Outline each Plasmodium malariae-infected red blood cell.
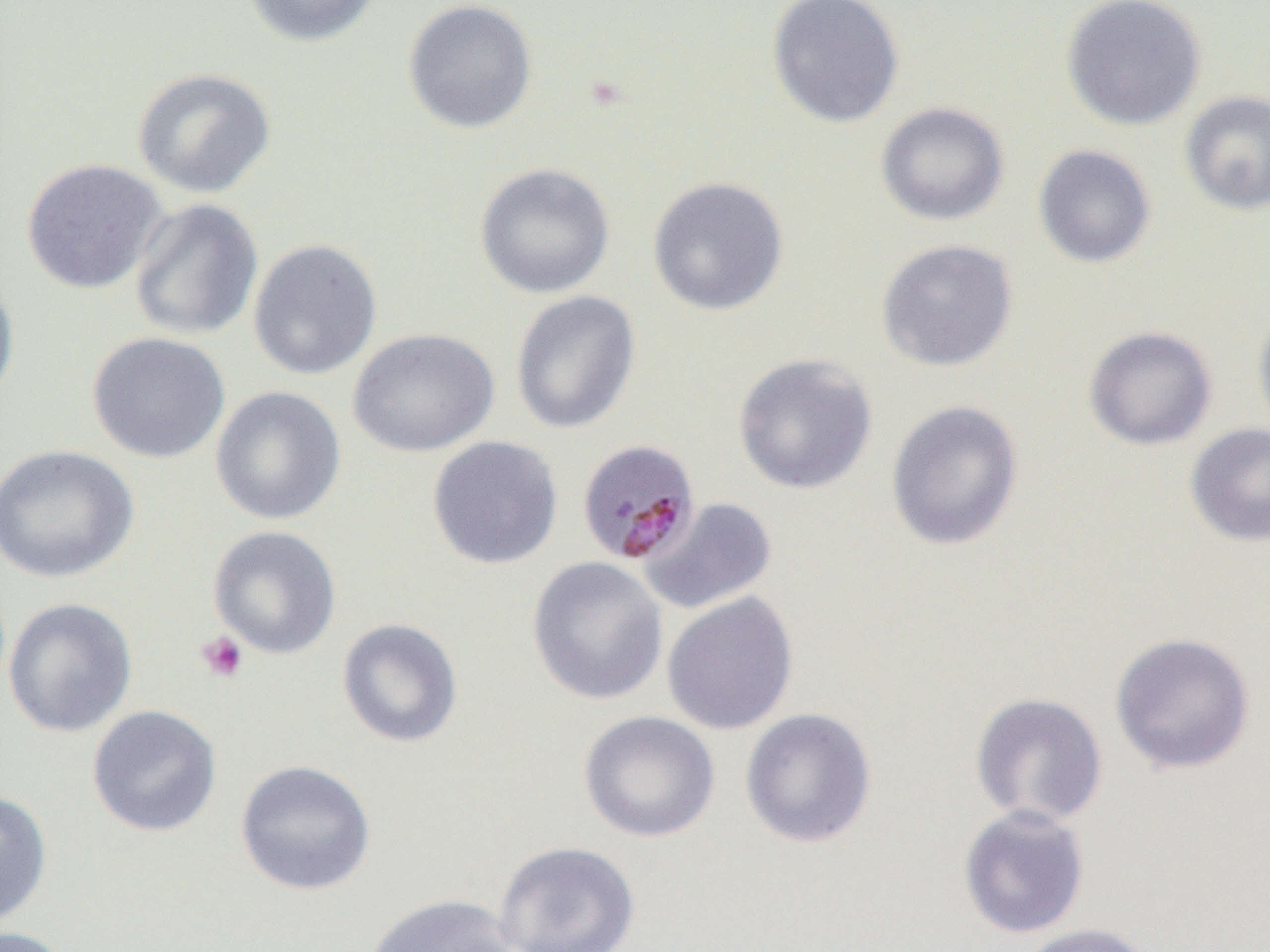
Approximate bounding boxes as named x1/y1/x2/y2 corners in pixels.
Plasmodium malariae-infected red blood cells: (x1=576, y1=438, x2=701, y2=565).

slide-level diagnosis = Plasmodium malariae
preparation = thin blood smear
magnification = 1000x
field of view = one of a larger specimen
image size = 1270×952 pixels
uninfected red blood cell locations = approximate bounding boxes as named x1/y1/x2/y2 corners in pixels: (x1=243, y1=0, x2=383, y2=48), (x1=402, y1=0, x2=538, y2=134), (x1=766, y1=0, x2=905, y2=128), (x1=1060, y1=0, x2=1206, y2=131), (x1=131, y1=67, x2=277, y2=199), (x1=1180, y1=90, x2=1270, y2=217), (x1=875, y1=101, x2=1010, y2=226), (x1=1032, y1=144, x2=1156, y2=268), (x1=21, y1=158, x2=168, y2=294), (x1=473, y1=163, x2=615, y2=299), (x1=647, y1=176, x2=789, y2=316), (x1=129, y1=198, x2=263, y2=341), (x1=248, y1=238, x2=382, y2=380), (x1=876, y1=238, x2=1019, y2=373), (x1=0, y1=271, x2=20, y2=411), (x1=510, y1=291, x2=641, y2=434), (x1=1252, y1=302, x2=1270, y2=440), (x1=1082, y1=325, x2=1217, y2=450), (x1=348, y1=327, x2=500, y2=458), (x1=87, y1=332, x2=231, y2=464), (x1=731, y1=352, x2=878, y2=495), (x1=210, y1=385, x2=347, y2=525), (x1=885, y1=399, x2=1024, y2=551), (x1=1185, y1=423, x2=1270, y2=546), (x1=427, y1=436, x2=563, y2=570), (x1=0, y1=444, x2=138, y2=583), (x1=638, y1=497, x2=779, y2=615), (x1=208, y1=525, x2=342, y2=659), (x1=526, y1=556, x2=668, y2=705), (x1=661, y1=591, x2=799, y2=735), (x1=3, y1=597, x2=138, y2=738), (x1=336, y1=617, x2=464, y2=748), (x1=1109, y1=631, x2=1256, y2=775), (x1=970, y1=692, x2=1108, y2=827), (x1=87, y1=705, x2=222, y2=837), (x1=740, y1=707, x2=877, y2=848), (x1=577, y1=710, x2=721, y2=843), (x1=234, y1=759, x2=376, y2=895), (x1=0, y1=788, x2=53, y2=929), (x1=957, y1=804, x2=1091, y2=940), (x1=493, y1=840, x2=641, y2=952), (x1=365, y1=893, x2=519, y2=952), (x1=1018, y1=922, x2=1154, y2=952), (x1=0, y1=925, x2=75, y2=952)
platelet locations = approximate bounding boxes as named x1/y1/x2/y2 corners in pixels: (x1=194, y1=631, x2=249, y2=683)
modality = optical microscopy